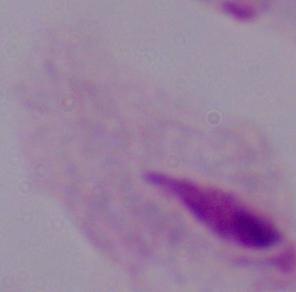

magnification: 1000x
modality: micrograph
identification: trichomonad